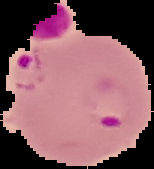
Summary:
  - Image size: 154×169 pixels
  - Image type: segmented cell region on a black background
  - Preparation: thin blood film
  - Result: malaria parasites detected